Locate and identify every blood parasite.
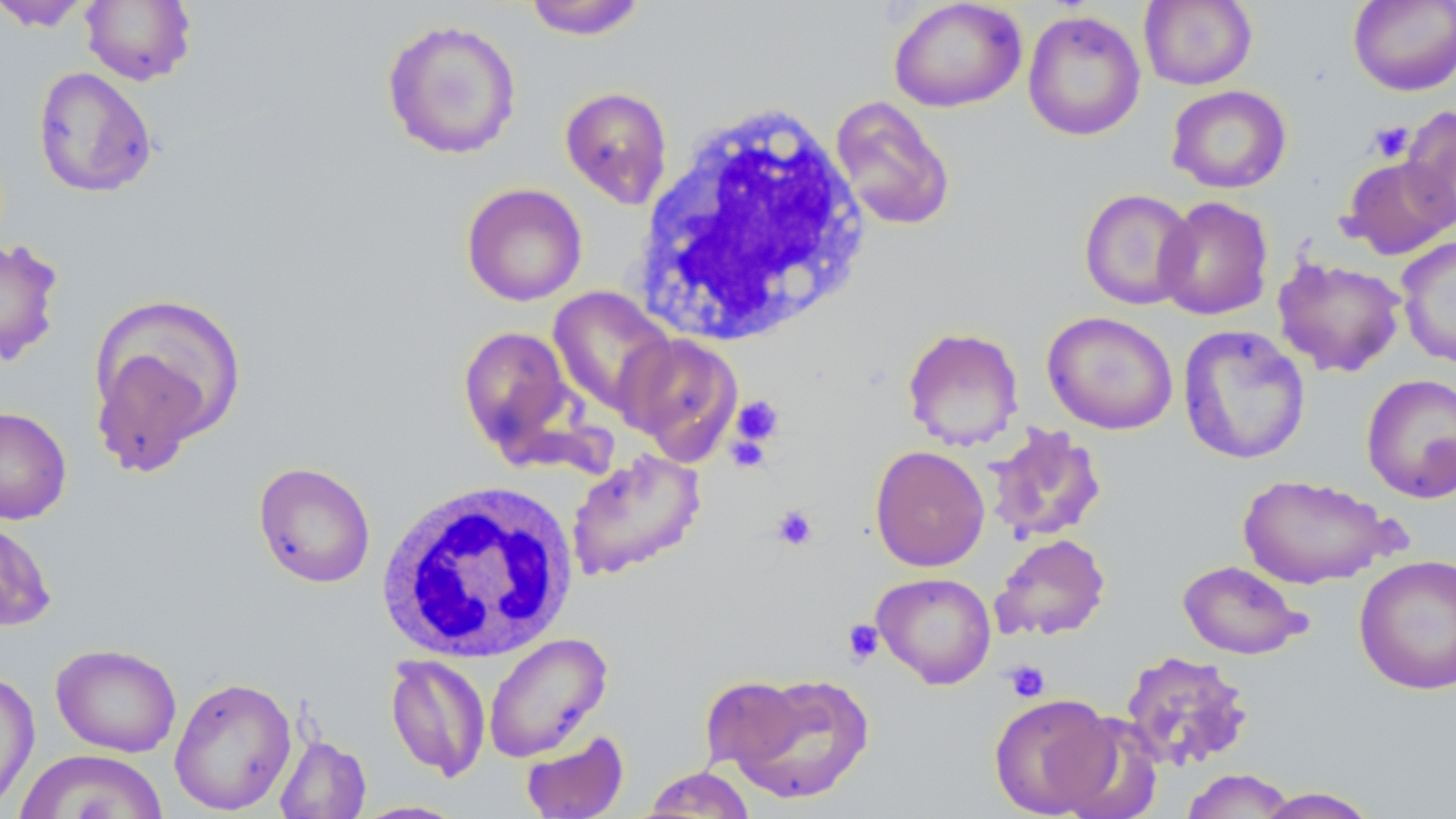

No blood parasites observed.

Summary:
  - Coordinate format: approximate bounding boxes as (x1, y1, x2, y2) in pixels
  - Uninfected red blood cell locations: (80, 0, 196, 86), (522, 0, 648, 40), (1140, 0, 1257, 90), (1348, 0, 1456, 96), (0, 1, 95, 32), (889, 1, 1027, 112), (1022, 9, 1146, 141), (381, 18, 522, 160), (32, 67, 157, 198), (559, 85, 673, 208), (1166, 85, 1292, 194), (829, 95, 956, 232), (1400, 105, 1456, 233), (1341, 157, 1456, 259), (460, 183, 588, 306), (1079, 188, 1198, 310), (1155, 196, 1274, 320), (1397, 236, 1456, 368), (0, 238, 64, 368), (1273, 256, 1406, 377), (547, 286, 675, 417), (87, 290, 248, 474), (1042, 311, 1178, 435), (1177, 324, 1311, 465), (458, 325, 579, 458), (901, 327, 1024, 451), (617, 332, 743, 462), (1361, 373, 1456, 504), (0, 406, 72, 524), (984, 423, 1108, 544), (871, 437, 1107, 558), (869, 445, 990, 572), (566, 449, 706, 580), (252, 461, 376, 589), (1237, 473, 1396, 589), (0, 517, 57, 633), (991, 533, 1111, 641), (1353, 554, 1456, 695), (1177, 559, 1309, 660), (871, 572, 996, 688), (484, 633, 612, 762), (50, 642, 182, 757), (1119, 649, 1254, 771), (385, 655, 490, 782), (0, 668, 39, 812), (718, 672, 875, 805), (169, 676, 297, 815), (988, 692, 1118, 817), (1053, 714, 1163, 819), (520, 729, 630, 819), (274, 734, 371, 818), (13, 749, 168, 819), (640, 766, 757, 817), (1181, 769, 1297, 818), (1251, 787, 1380, 817), (350, 800, 469, 819)
  - Platelet locations: (1368, 121, 1415, 162), (731, 395, 784, 448), (772, 505, 818, 551), (842, 619, 884, 666), (1004, 660, 1050, 703)
  - White blood cell locations: (634, 99, 872, 346), (377, 479, 578, 664)
  - Slide-level diagnosis: no evidence of blood parasites
  - Stain: May-Grünwald-Giemsa
  - Modality: optical microscopy
  - Magnification: 1000x
  - Image size: 1456×819 pixels
  - Field of view: single
  - Preparation: thin blood smear